Classify this cell by malaria status.
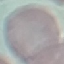
It is uninfected.

Acquired by smartphone through the microscope eyepiece. Automatically extracted cell patch, resized to 64 × 64 pixels. Thin smear of blood. Giemsa stain.